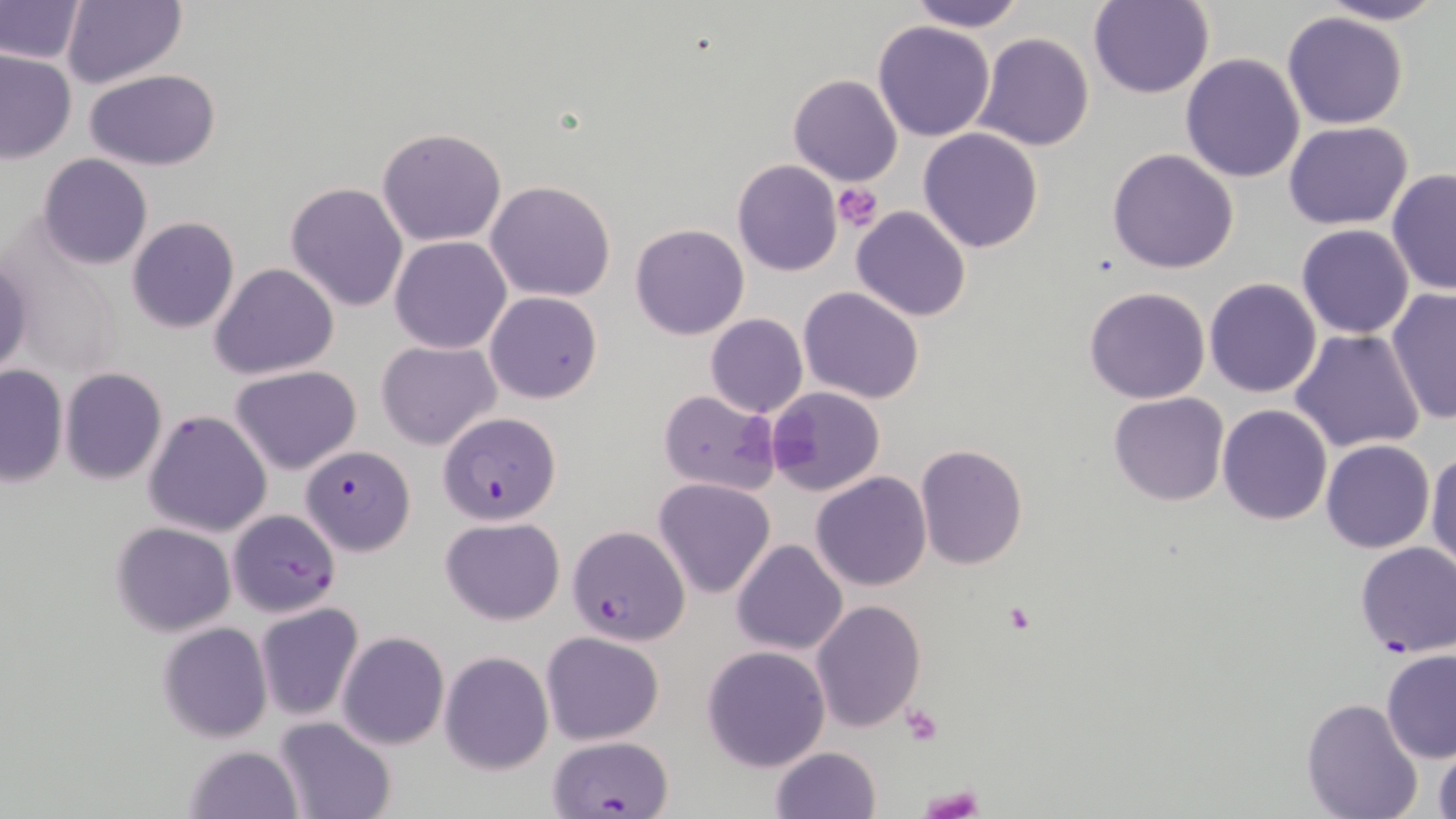

Approximate bounding boxes as (x1, y1, x2, y2) in pixels. Platelet locations: (833, 183, 883, 231), (1004, 603, 1033, 632), (900, 704, 943, 745), (919, 782, 983, 816). Uninfected red blood cell locations: (906, 0, 1027, 31), (1088, 0, 1214, 99), (1316, 0, 1446, 25), (1, 1, 86, 65), (61, 2, 186, 87), (1282, 10, 1408, 129), (873, 21, 995, 142), (972, 34, 1093, 152), (0, 48, 76, 162), (1181, 53, 1306, 183), (84, 68, 221, 171), (788, 74, 903, 187), (1283, 120, 1413, 229), (918, 126, 1044, 254), (377, 127, 507, 246), (1107, 149, 1239, 274), (38, 154, 152, 270), (731, 159, 843, 276), (1386, 167, 1455, 296), (486, 180, 617, 302), (285, 181, 410, 313), (850, 204, 973, 321), (127, 217, 240, 335), (630, 223, 749, 341), (1297, 223, 1415, 338), (390, 236, 511, 354), (0, 252, 32, 383), (209, 262, 339, 381), (1204, 277, 1321, 398), (798, 286, 925, 403), (1085, 287, 1211, 404), (1385, 289, 1455, 426), (485, 291, 602, 404), (705, 313, 808, 418), (1290, 329, 1425, 453), (376, 339, 500, 450), (0, 365, 68, 487), (230, 365, 362, 475), (60, 367, 166, 483), (767, 386, 885, 496), (657, 390, 781, 495), (1109, 392, 1229, 507), (1216, 404, 1333, 525), (143, 409, 273, 537), (1321, 438, 1436, 553), (915, 444, 1028, 569), (1427, 450, 1456, 573), (811, 471, 930, 591), (653, 478, 775, 599), (441, 516, 565, 624), (111, 522, 237, 635), (731, 539, 849, 655), (810, 600, 926, 734), (254, 603, 365, 721), (749, 606, 916, 779), (158, 623, 272, 743), (336, 631, 450, 750), (541, 631, 665, 745), (701, 644, 831, 772), (440, 651, 553, 774), (1380, 651, 1456, 765), (1302, 696, 1423, 819), (273, 717, 397, 819), (1431, 737, 1456, 819), (185, 743, 305, 819), (770, 746, 881, 819). Plasmodium falciparum-infected red blood cell locations: (437, 411, 562, 525), (301, 445, 415, 557), (227, 509, 341, 616), (569, 524, 689, 646), (1354, 541, 1456, 657), (549, 744, 675, 819). Slide-level diagnosis: Plasmodium falciparum. Thin blood film. Single field of view. Optical microscopy. Captured at 1000x magnification. Image is 1456×819 pixels. May-Grünwald-Giemsa stain.